Assess the morphology of the red blood cells.
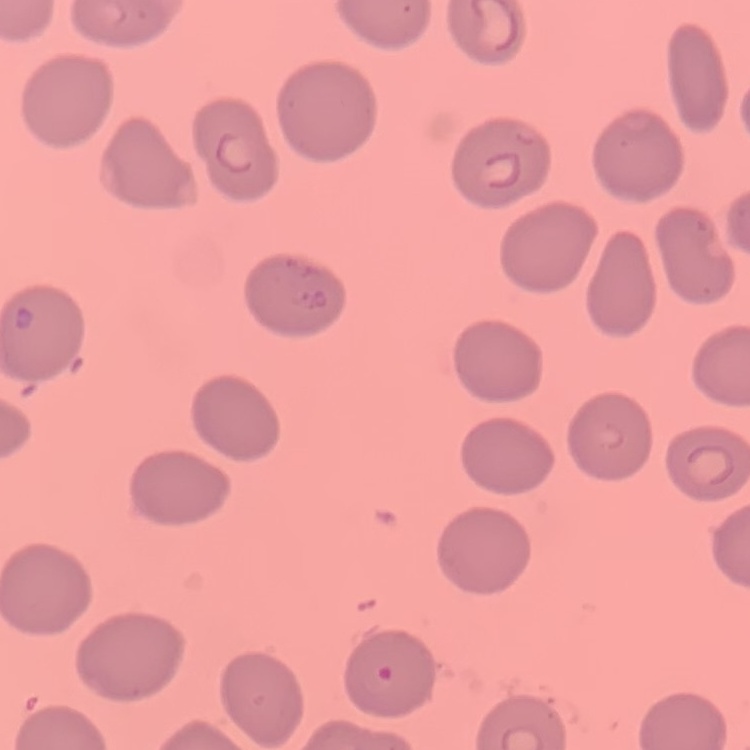
No rouleaux formation.

image_type: one tile cut from a larger photomicrograph
preparation: thin blood smear
stain: Field's or Giemsa